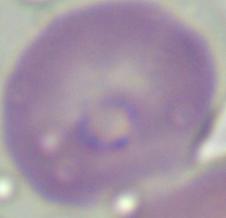

1000x magnification. Micrograph. A Babesia parasite is seen.